Report the malaria status of this cell.
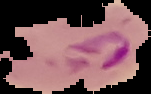
It is parasitized.

image size = 151×94 pixels
preparation = thin blood smear
image type = segmented cell region on a black background